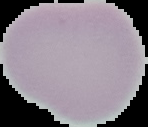
Malaria status: uninfected. Segmented cell region on a black background. Image is 148×127 pixels. From a thin blood film.